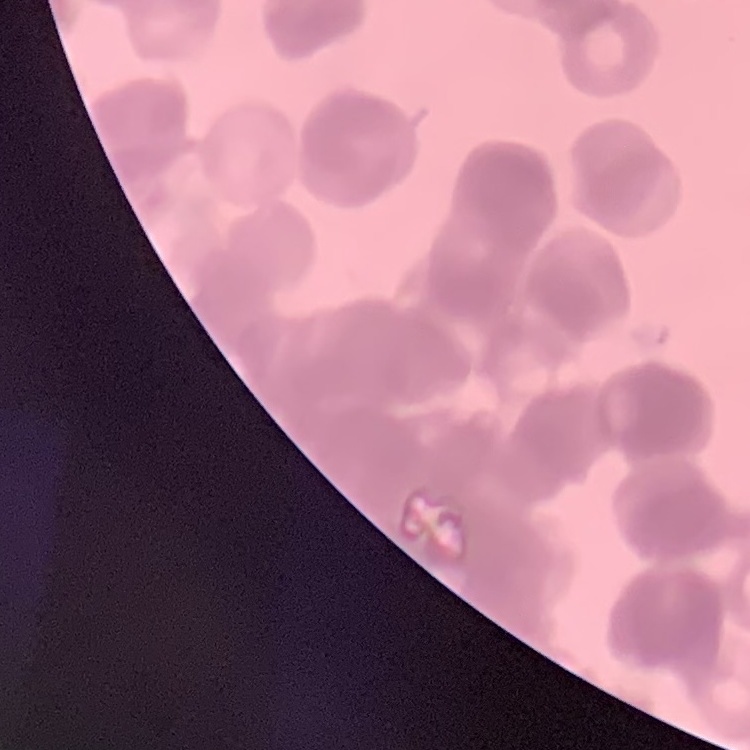

red blood cell morphology = rouleaux formation
stain = Field's or Giemsa
preparation = thin peripheral smear
image type = square crop of a larger photomicrograph